Point out each leukocyte.
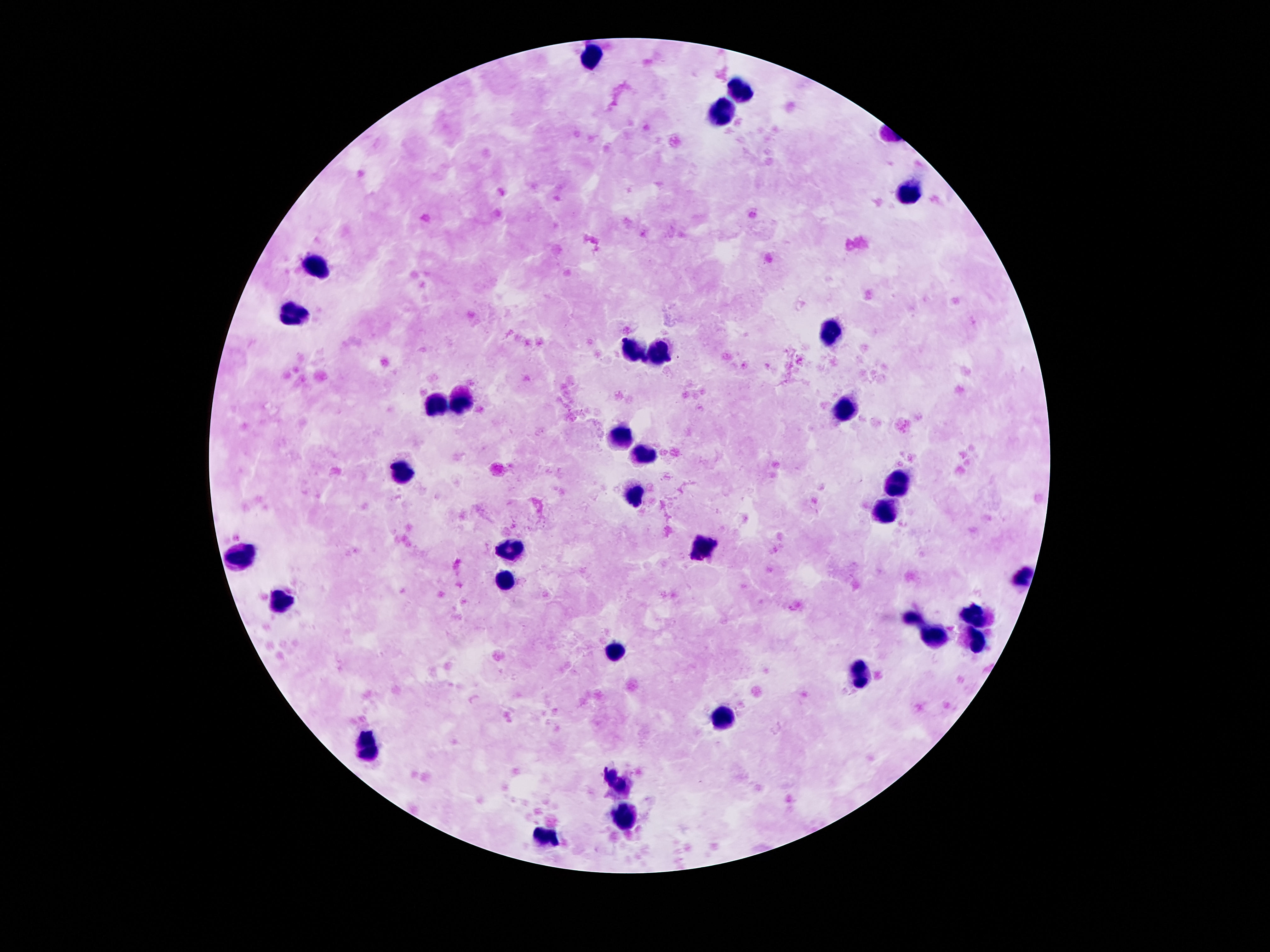
Approximate centers as [x, y] in pixels.
Leukocytes: [592, 54], [743, 89], [720, 113], [908, 195], [318, 268], [295, 313], [831, 330], [634, 348], [658, 350], [463, 400], [440, 404], [851, 405], [622, 439], [643, 454], [402, 470], [897, 475], [636, 497], [883, 509], [511, 545], [702, 548], [243, 557], [506, 577], [1024, 577], [281, 598], [974, 614], [911, 616], [936, 638], [976, 643], [617, 652], [865, 670], [726, 714], [366, 745], [620, 777], [625, 813], [545, 838].

Photographed through the microscope eyepiece with a smartphone camera. Patient malaria status: negative. One field from this slide. Image is 1270×952 pixels. 100x magnification. Thick blood film. Giemsa stain.